Name the parasite shown.
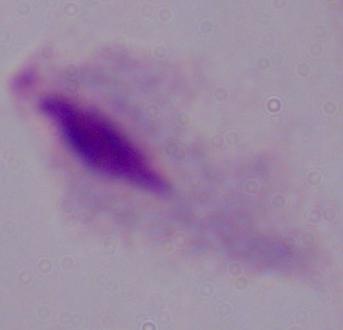
This is a trichomonad.

Summary:
  - Magnification: 1000x
  - Modality: photomicrograph